State the blood parasite species.
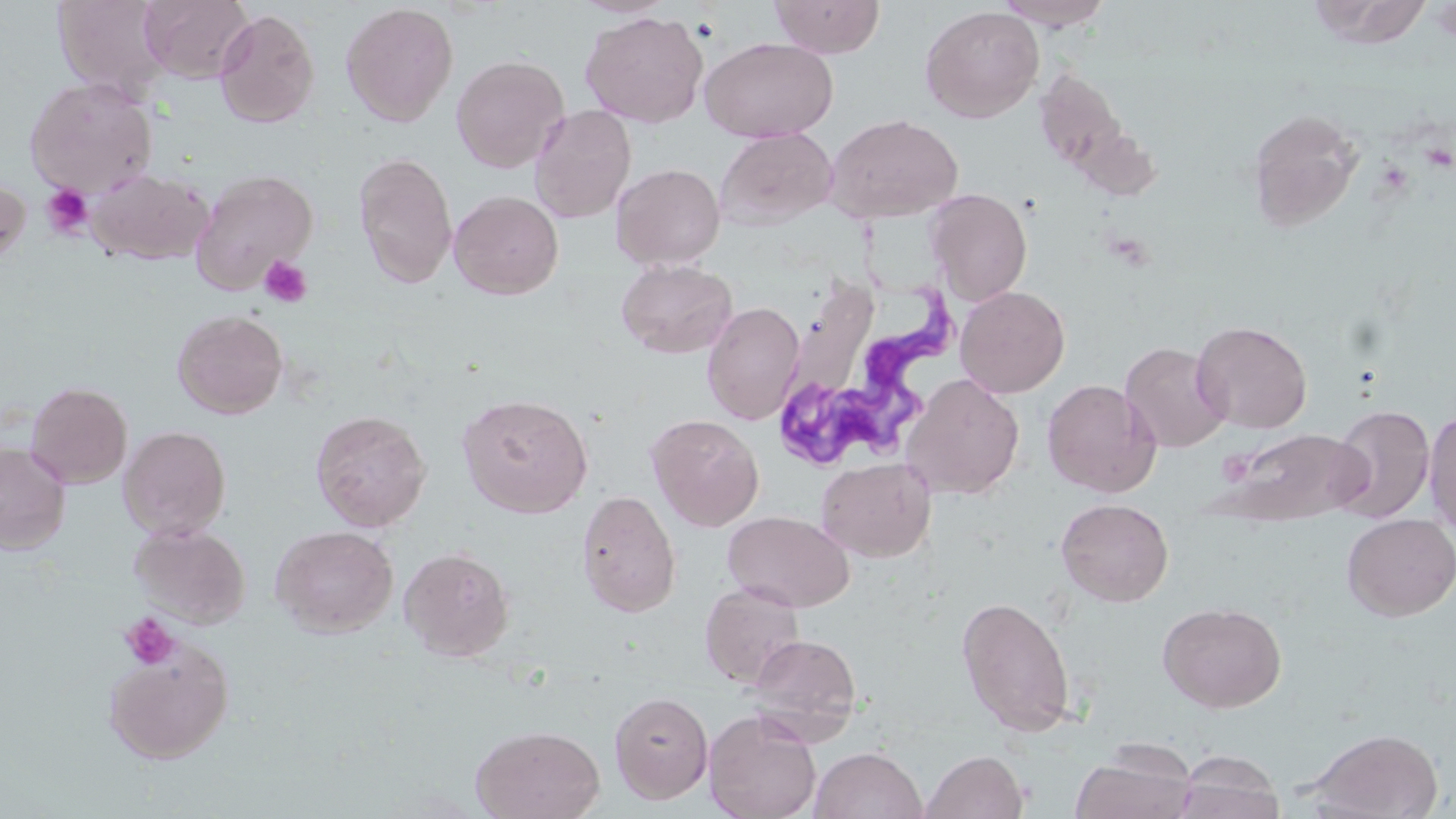
Trypanosoma brucei.

Summary:
  - Coordinate format: approximate bounding boxes as [x1, y1, x2, y2] in pixels
  - Trypanosoma brucei locations: [768, 276, 965, 477]
  - Uninfected red blood cell locations: [53, 0, 171, 100], [140, 0, 252, 83], [768, 0, 886, 58], [994, 0, 1116, 30], [1310, 0, 1436, 49], [340, 2, 458, 126], [920, 5, 1045, 123], [213, 9, 319, 129], [580, 10, 709, 128], [698, 36, 838, 143], [450, 54, 570, 173], [1034, 67, 1130, 177], [24, 77, 158, 199], [529, 105, 636, 223], [1246, 108, 1364, 232], [824, 113, 963, 224], [716, 127, 838, 230], [353, 152, 458, 289], [611, 163, 725, 270], [88, 168, 212, 265], [190, 169, 318, 294], [0, 174, 31, 269], [924, 188, 1033, 305], [449, 190, 564, 300], [615, 258, 737, 359], [784, 279, 892, 410], [955, 285, 1070, 398], [702, 301, 805, 425], [172, 308, 288, 419], [1191, 320, 1312, 433], [1119, 341, 1232, 453], [901, 372, 1025, 500], [1041, 378, 1161, 498], [26, 382, 133, 488], [457, 392, 594, 518], [1328, 404, 1436, 524], [1424, 407, 1456, 539], [310, 408, 432, 532], [646, 413, 765, 531], [118, 425, 231, 539], [1222, 427, 1369, 524], [0, 442, 70, 553], [816, 457, 935, 562], [576, 489, 681, 618], [1056, 498, 1174, 607], [722, 509, 855, 612], [1341, 513, 1456, 621], [129, 523, 250, 628], [270, 524, 399, 637], [398, 546, 515, 661], [699, 581, 805, 688], [955, 595, 1076, 738], [1157, 601, 1287, 713], [748, 633, 862, 737], [104, 643, 233, 764], [609, 691, 713, 803], [704, 709, 822, 819], [471, 723, 605, 819], [1304, 727, 1444, 818], [810, 746, 927, 819], [1070, 747, 1197, 819], [1173, 748, 1286, 819], [921, 749, 1029, 819]
  - Platelet locations: [41, 184, 94, 238], [258, 255, 313, 308], [120, 613, 180, 670]
  - Field of view: single
  - Image size: 1456×819 pixels
  - Magnification: 1000x
  - Modality: optical microscopy
  - Stain: May-Grünwald-Giemsa
  - Preparation: thin blood film